Classify this cell by malaria status.
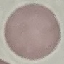
It is uninfected.

image type = automatically extracted cell patch, resized to 64 × 64 pixels
stain = Giemsa
capture = smartphone through the microscope eyepiece
preparation = thin blood film